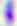

Toxoplasma gondii is shown. Photomicrograph. Captured at 400x magnification.